Describe the morphology of the erythrocytes.
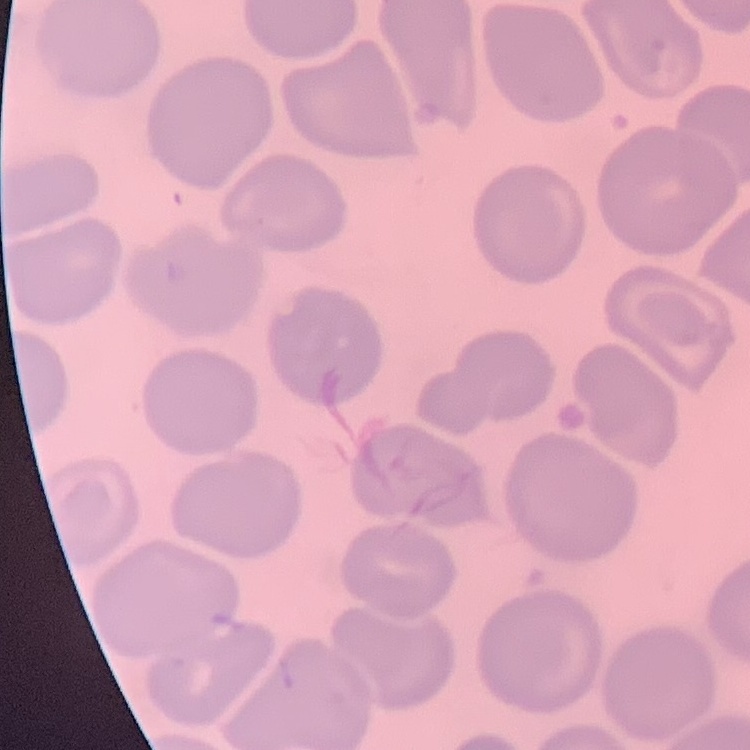
No rouleaux formation.

Thin blood film. One tile cut from a larger photomicrograph. Field's or Giemsa stain.